Report the malaria status of this cell.
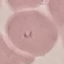

It is parasitized.

Thin blood film. Cell patch, automatically extracted from a larger field of view and resized to 64 × 64 pixels. Giemsa stain. Photographed with a smartphone camera at the microscope eyepiece.